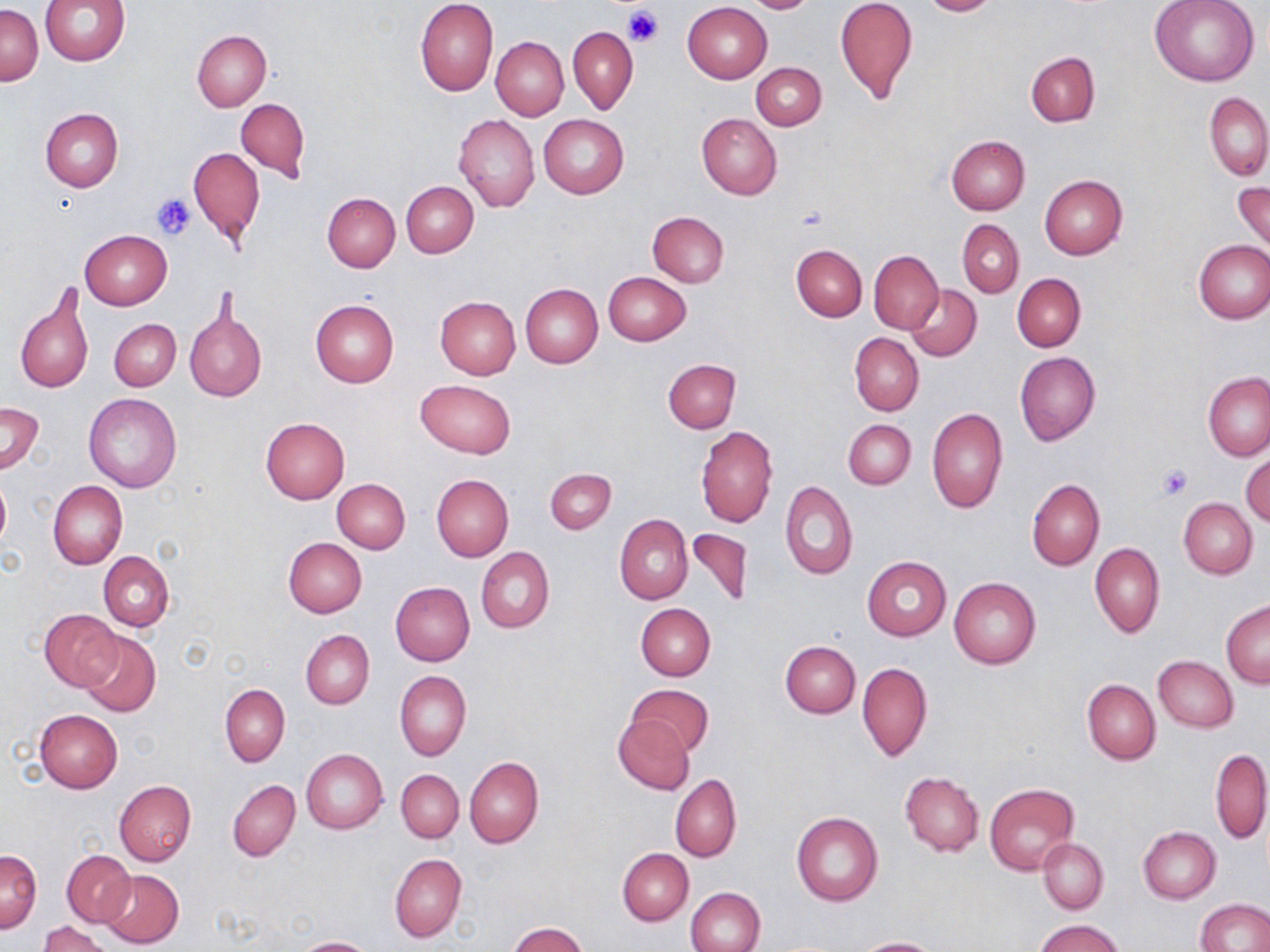

slide-level diagnosis = no evidence of blood parasites
uninfected red blood cell locations = approximate bounding boxes as named x1/y1/x2/y2 corners in pixels: (x1=40, y1=0, x2=131, y2=65), (x1=414, y1=0, x2=498, y2=97), (x1=742, y1=0, x2=823, y2=14), (x1=834, y1=0, x2=918, y2=104), (x1=918, y1=0, x2=1001, y2=16), (x1=1151, y1=0, x2=1259, y2=86), (x1=682, y1=3, x2=772, y2=83), (x1=1, y1=4, x2=43, y2=86), (x1=568, y1=26, x2=637, y2=115), (x1=192, y1=29, x2=271, y2=110), (x1=491, y1=36, x2=569, y2=121), (x1=1026, y1=52, x2=1100, y2=126), (x1=752, y1=63, x2=826, y2=130), (x1=1205, y1=91, x2=1270, y2=182), (x1=236, y1=98, x2=311, y2=181), (x1=41, y1=109, x2=123, y2=191), (x1=454, y1=114, x2=539, y2=212), (x1=696, y1=114, x2=782, y2=199), (x1=538, y1=115, x2=629, y2=198), (x1=947, y1=135, x2=1030, y2=215), (x1=188, y1=146, x2=264, y2=246), (x1=1039, y1=175, x2=1128, y2=259), (x1=1233, y1=179, x2=1270, y2=255), (x1=401, y1=181, x2=477, y2=257), (x1=322, y1=193, x2=400, y2=272), (x1=646, y1=211, x2=729, y2=287), (x1=957, y1=219, x2=1023, y2=297), (x1=80, y1=229, x2=172, y2=309), (x1=1193, y1=239, x2=1270, y2=323), (x1=791, y1=244, x2=867, y2=320), (x1=869, y1=250, x2=944, y2=333), (x1=603, y1=272, x2=691, y2=345), (x1=1013, y1=273, x2=1085, y2=351), (x1=520, y1=283, x2=603, y2=368), (x1=906, y1=283, x2=982, y2=360), (x1=15, y1=288, x2=94, y2=395), (x1=435, y1=296, x2=520, y2=379), (x1=310, y1=300, x2=399, y2=387), (x1=185, y1=308, x2=266, y2=401), (x1=108, y1=318, x2=181, y2=391), (x1=849, y1=333, x2=923, y2=416), (x1=1015, y1=352, x2=1100, y2=446), (x1=663, y1=358, x2=740, y2=433), (x1=1204, y1=371, x2=1269, y2=461), (x1=415, y1=378, x2=515, y2=457), (x1=83, y1=393, x2=182, y2=492), (x1=0, y1=402, x2=44, y2=473), (x1=926, y1=408, x2=1008, y2=514), (x1=261, y1=417, x2=349, y2=503), (x1=843, y1=419, x2=916, y2=489), (x1=696, y1=426, x2=778, y2=529), (x1=1241, y1=450, x2=1270, y2=527), (x1=545, y1=468, x2=616, y2=534), (x1=431, y1=474, x2=513, y2=562), (x1=0, y1=475, x2=10, y2=550), (x1=332, y1=478, x2=410, y2=553), (x1=1027, y1=479, x2=1104, y2=571), (x1=48, y1=480, x2=127, y2=570), (x1=781, y1=482, x2=858, y2=580), (x1=1178, y1=498, x2=1257, y2=578), (x1=615, y1=515, x2=693, y2=605), (x1=686, y1=529, x2=751, y2=609), (x1=283, y1=537, x2=367, y2=617), (x1=1090, y1=543, x2=1164, y2=638), (x1=477, y1=548, x2=554, y2=633), (x1=99, y1=551, x2=174, y2=631), (x1=862, y1=556, x2=952, y2=641), (x1=949, y1=577, x2=1041, y2=669), (x1=390, y1=582, x2=474, y2=666), (x1=1221, y1=599, x2=1270, y2=687), (x1=635, y1=602, x2=716, y2=680), (x1=39, y1=608, x2=122, y2=690), (x1=301, y1=630, x2=374, y2=708), (x1=78, y1=631, x2=161, y2=718), (x1=781, y1=640, x2=860, y2=718), (x1=1153, y1=656, x2=1238, y2=732), (x1=857, y1=661, x2=932, y2=761), (x1=395, y1=671, x2=471, y2=762), (x1=1083, y1=679, x2=1160, y2=765), (x1=625, y1=683, x2=713, y2=755), (x1=220, y1=685, x2=289, y2=766), (x1=33, y1=708, x2=123, y2=792), (x1=614, y1=716, x2=695, y2=794), (x1=301, y1=748, x2=387, y2=833), (x1=1211, y1=748, x2=1269, y2=843), (x1=465, y1=756, x2=544, y2=847), (x1=396, y1=769, x2=464, y2=842), (x1=900, y1=771, x2=983, y2=856), (x1=671, y1=773, x2=742, y2=862), (x1=114, y1=780, x2=196, y2=866), (x1=228, y1=780, x2=301, y2=862), (x1=985, y1=783, x2=1079, y2=874), (x1=791, y1=812, x2=883, y2=907), (x1=1138, y1=826, x2=1221, y2=903), (x1=1038, y1=838, x2=1108, y2=914), (x1=618, y1=848, x2=693, y2=925), (x1=63, y1=850, x2=135, y2=926), (x1=0, y1=851, x2=41, y2=932), (x1=390, y1=853, x2=466, y2=943), (x1=98, y1=869, x2=183, y2=949), (x1=686, y1=886, x2=765, y2=952), (x1=1197, y1=899, x2=1269, y2=952), (x1=1036, y1=919, x2=1124, y2=952), (x1=38, y1=921, x2=113, y2=952), (x1=506, y1=922, x2=588, y2=952), (x1=293, y1=937, x2=378, y2=952), (x1=855, y1=937, x2=940, y2=952)
modality = light microscopy
preparation = thin blood film
image size = 1270×952 pixels
field of view = single
stain = May-Grünwald-Giemsa
platelet locations = approximate bounding boxes as named x1/y1/x2/y2 corners in pixels: (x1=623, y1=5, x2=664, y2=46), (x1=151, y1=193, x2=196, y2=241), (x1=796, y1=206, x2=829, y2=231), (x1=1156, y1=464, x2=1192, y2=501)
magnification = 1000x